State which parasite is depicted.
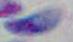

This is Toxoplasma gondii.

Summary:
  - Modality: micrograph
  - Magnification: 1000x